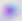 400x magnification. Toxoplasma gondii is seen. Micrograph.